Give the preparation type.
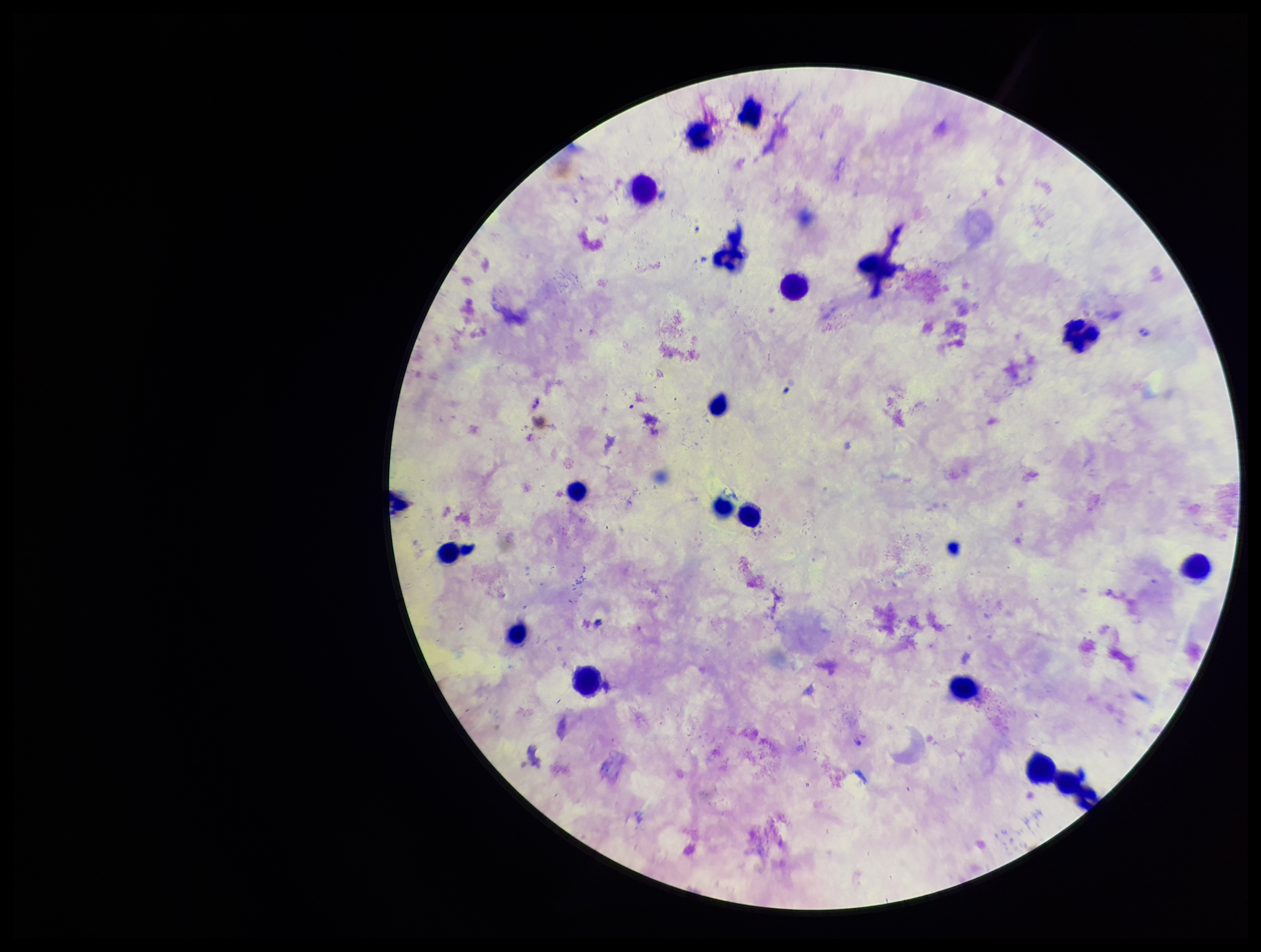

It is a thick blood smear.

Summary:
  - Capture: smartphone photograph through the microscope eyepiece
  - Field of view: single
  - Parasite count: 0
  - Patient malaria status: positive
  - Stain: Giemsa
  - Species reported for this patient: Plasmodium falciparum
  - Leukocyte count: 18
  - Image size: 1261×952 pixels
  - Plasmodium parasites: none seen